Give the position of every malaria parasite.
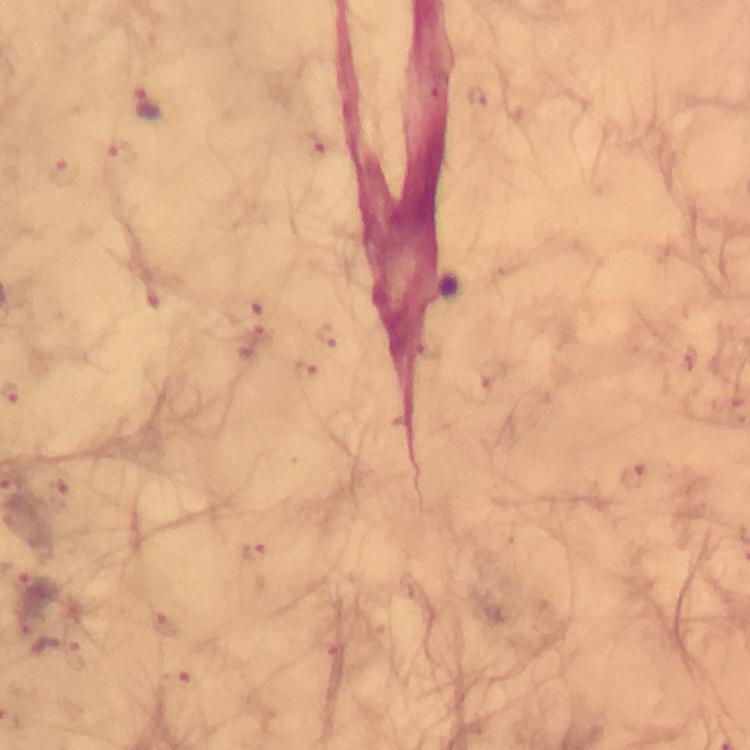

Approximate centers as (x, y) in pixels.
Malaria parasites: (480, 96), (149, 104), (122, 156), (64, 175), (632, 477), (254, 552), (28, 588), (56, 648).

Summary:
  - Immersion oil: applied
  - Magnification: 100x
  - Stain: Giemsa
  - Preparation: thick blood smear
  - Capture: smartphone mounted on the microscope
  - Cropped from: one field of view
  - Image size: 750×750 pixels
  - Context: from a diagnostic examination for malaria